Identify the parasite.
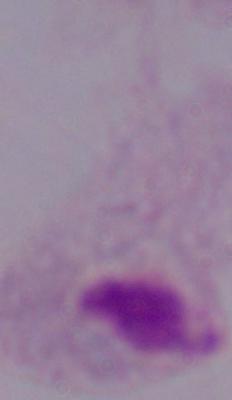
This is a trichomonad.

Summary:
  - Modality: photomicrograph
  - Magnification: 1000x